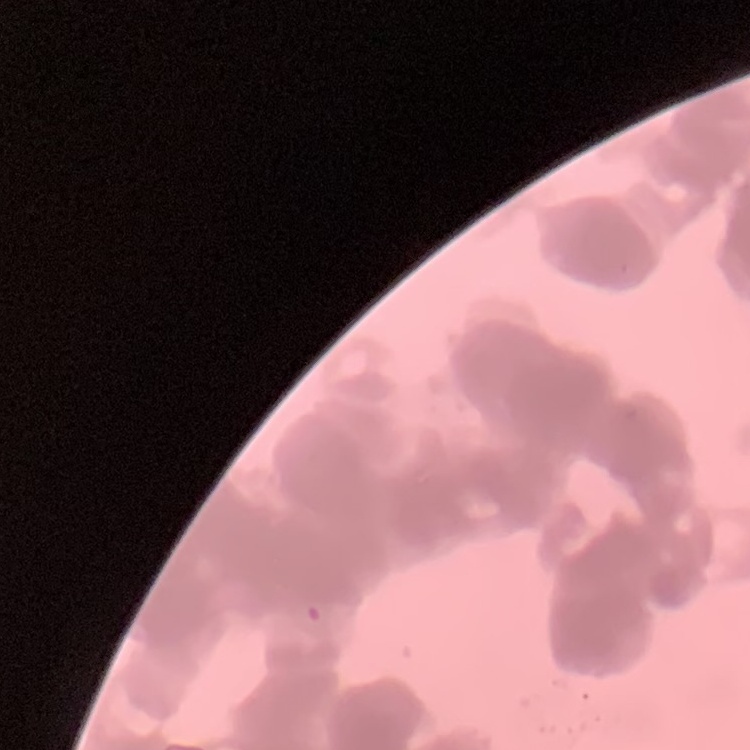

The erythrocytes exhibit rouleaux formation. Thin blood smear. Square crop of a larger photomicrograph. Stained with either Field's or Giemsa.